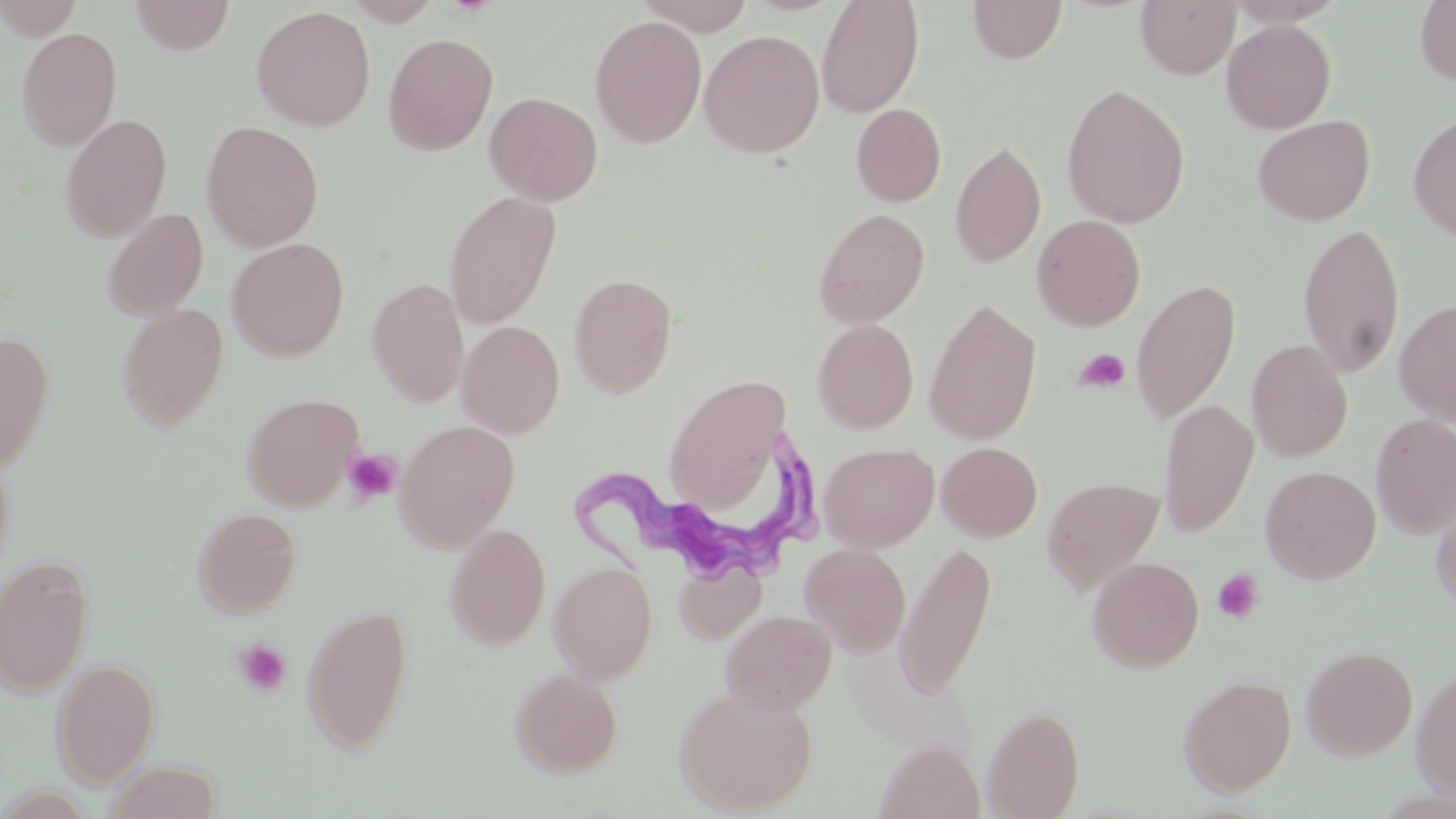
slide-level diagnosis = Trypanosoma brucei
stain = May-Grünwald-Giemsa
modality = optical microscopy
uninfected red blood cell locations = approximate bounding boxes as named x1/y1/x2/y2 corners in pixels: (x1=0, y1=0, x2=83, y2=40), (x1=129, y1=0, x2=236, y2=55), (x1=340, y1=0, x2=445, y2=26), (x1=635, y1=0, x2=756, y2=35), (x1=816, y1=0, x2=925, y2=117), (x1=967, y1=0, x2=1068, y2=64), (x1=1415, y1=0, x2=1456, y2=87), (x1=1135, y1=1, x2=1240, y2=79), (x1=251, y1=6, x2=375, y2=130), (x1=589, y1=14, x2=707, y2=148), (x1=1221, y1=19, x2=1336, y2=133), (x1=16, y1=27, x2=122, y2=152), (x1=699, y1=29, x2=824, y2=158), (x1=383, y1=32, x2=499, y2=156), (x1=1061, y1=84, x2=1190, y2=229), (x1=484, y1=92, x2=603, y2=206), (x1=850, y1=103, x2=946, y2=207), (x1=1408, y1=111, x2=1456, y2=242), (x1=58, y1=112, x2=173, y2=241), (x1=1251, y1=114, x2=1375, y2=226), (x1=200, y1=121, x2=324, y2=252), (x1=950, y1=140, x2=1046, y2=268), (x1=443, y1=190, x2=562, y2=328), (x1=100, y1=208, x2=209, y2=320), (x1=813, y1=208, x2=930, y2=328), (x1=1031, y1=214, x2=1146, y2=331), (x1=1297, y1=223, x2=1406, y2=381), (x1=227, y1=238, x2=349, y2=361), (x1=568, y1=273, x2=678, y2=397), (x1=366, y1=278, x2=469, y2=407), (x1=1130, y1=280, x2=1241, y2=424), (x1=1394, y1=297, x2=1456, y2=426), (x1=924, y1=299, x2=1041, y2=445), (x1=115, y1=304, x2=229, y2=432), (x1=812, y1=319, x2=919, y2=433), (x1=456, y1=320, x2=565, y2=437), (x1=0, y1=331, x2=55, y2=472), (x1=1246, y1=340, x2=1353, y2=462), (x1=664, y1=373, x2=793, y2=513), (x1=241, y1=392, x2=364, y2=511), (x1=1159, y1=399, x2=1258, y2=536), (x1=1371, y1=413, x2=1456, y2=538), (x1=395, y1=419, x2=520, y2=551), (x1=0, y1=441, x2=15, y2=585), (x1=819, y1=442, x2=939, y2=552), (x1=936, y1=442, x2=1043, y2=541), (x1=1260, y1=465, x2=1381, y2=583), (x1=1042, y1=476, x2=1163, y2=595), (x1=1429, y1=486, x2=1456, y2=613), (x1=192, y1=507, x2=303, y2=617), (x1=445, y1=523, x2=551, y2=649), (x1=895, y1=541, x2=997, y2=698), (x1=799, y1=543, x2=911, y2=656), (x1=0, y1=554, x2=95, y2=697), (x1=1087, y1=556, x2=1204, y2=672), (x1=673, y1=558, x2=766, y2=643), (x1=549, y1=561, x2=658, y2=683), (x1=301, y1=602, x2=414, y2=755), (x1=720, y1=609, x2=836, y2=715), (x1=1300, y1=644, x2=1418, y2=759), (x1=51, y1=658, x2=161, y2=786), (x1=1411, y1=664, x2=1456, y2=802), (x1=510, y1=666, x2=623, y2=776), (x1=1178, y1=674, x2=1296, y2=796), (x1=674, y1=686, x2=818, y2=814), (x1=982, y1=704, x2=1085, y2=818), (x1=876, y1=740, x2=984, y2=819), (x1=103, y1=760, x2=223, y2=819)
preparation = thin blood smear
image size = 1456×819 pixels
platelet locations = approximate bounding boxes as named x1/y1/x2/y2 corners in pixels: (x1=1074, y1=349, x2=1130, y2=393), (x1=342, y1=448, x2=402, y2=505), (x1=1212, y1=568, x2=1264, y2=624), (x1=231, y1=638, x2=292, y2=698)
field of view = single
Trypanosoma brucei locations = approximate bounding boxes as named x1/y1/x2/y2 corners in pixels: (x1=572, y1=431, x2=820, y2=578)
magnification = 1000x